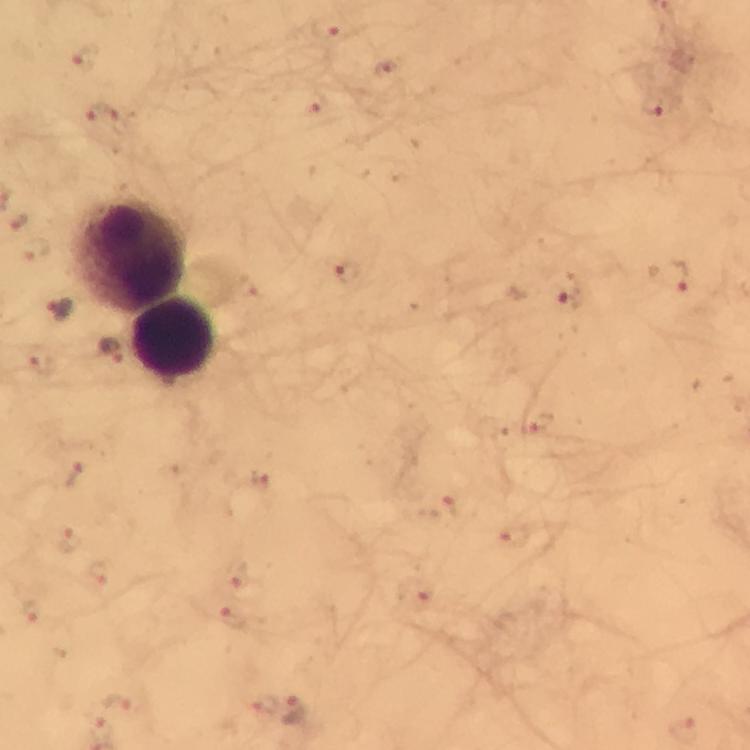

Approximate centers as (x, y) in pixels.
Summary:
  - Plasmodium parasite locations: (329, 29), (86, 56), (385, 69), (651, 107), (319, 110), (105, 116), (19, 221), (36, 250), (349, 273), (672, 277), (571, 297), (58, 310), (112, 353), (542, 422), (77, 475), (262, 480), (448, 508), (515, 537), (70, 539), (99, 572), (233, 575), (415, 594), (31, 614), (232, 617), (118, 701), (262, 702), (295, 712), (100, 727), (684, 730)
  - Leukocyte locations: (138, 254), (170, 339)
  - Magnification: 100x
  - Stain: Giemsa
  - Immersion oil: applied
  - Image size: 750×750 pixels
  - Capture: smartphone photograph through a microscope
  - Cropped from: one field of view
  - Preparation: thick blood film
  - Context: from a malaria diagnostic workup